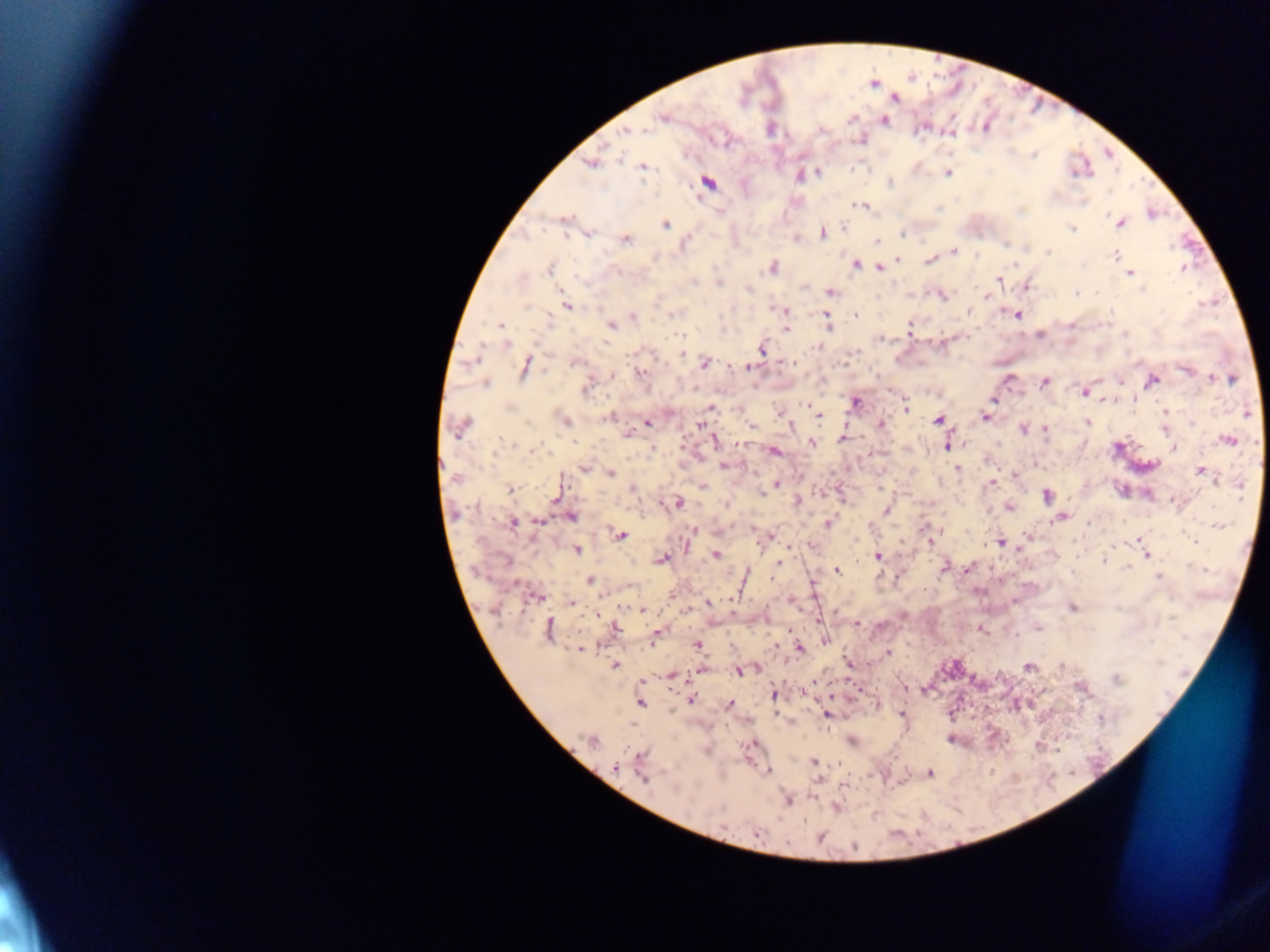

Approximate centers as [x, y] in pixels. Malaria parasite locations: [874, 84], [894, 97], [663, 118], [851, 118], [883, 120], [820, 130], [627, 131], [951, 132], [860, 139], [590, 162], [643, 166], [816, 172], [947, 172], [799, 175], [707, 182], [862, 205], [1151, 213], [564, 221], [1119, 222], [665, 224], [843, 225], [1072, 228], [586, 232], [821, 232], [901, 233], [624, 239], [796, 239], [876, 242], [953, 251], [1115, 255], [930, 259], [898, 260], [854, 264], [772, 267], [878, 267], [550, 268], [1184, 268], [1129, 273], [998, 279], [718, 282], [1027, 286], [830, 292], [941, 294], [987, 297], [566, 305], [783, 311], [968, 312], [856, 314], [1016, 314], [633, 316], [826, 318], [611, 325], [909, 326], [501, 327], [786, 328], [1040, 334], [879, 338], [505, 344], [762, 348], [474, 359], [791, 361], [574, 362], [704, 363], [750, 365], [524, 366], [1187, 369], [641, 373], [612, 375], [1211, 378], [1232, 378], [1009, 379], [1120, 381], [1152, 381], [1044, 382], [485, 384], [587, 385], [1084, 391], [1133, 398], [994, 399], [1103, 401], [855, 402], [709, 407], [906, 407], [781, 412], [1164, 413], [1247, 413], [817, 415], [611, 417], [985, 417], [564, 420], [937, 420], [647, 421], [1087, 423], [1192, 423], [640, 424], [880, 424], [700, 425], [460, 427], [750, 427], [1023, 427], [1045, 429], [628, 433], [842, 438], [1228, 440], [812, 441], [715, 442], [947, 444], [1173, 447], [654, 448], [774, 450], [725, 465], [584, 468], [957, 468], [1201, 471], [608, 473], [1014, 474], [992, 481], [776, 484], [701, 486], [771, 486], [633, 488], [510, 489], [1047, 494], [797, 501], [1176, 502], [675, 503], [726, 504], [1008, 507], [886, 509], [571, 515], [1058, 517], [512, 522], [828, 523], [694, 529], [620, 535], [768, 536], [1138, 538], [930, 540], [1194, 541], [1000, 542], [790, 545], [575, 549], [715, 554], [1146, 554], [878, 555], [661, 558], [1105, 561], [778, 562], [1128, 566], [945, 567], [968, 568], [837, 570], [1158, 575], [590, 580], [812, 588], [537, 595], [790, 599], [708, 602], [571, 603], [1072, 607], [642, 609], [686, 610], [856, 624], [1037, 628], [614, 629], [979, 629], [549, 630], [788, 631], [657, 635], [825, 640], [698, 645], [581, 648], [799, 648], [887, 653], [614, 664], [849, 665], [1061, 665], [1028, 666], [757, 668], [701, 670], [740, 670], [671, 675], [1115, 679], [813, 680], [641, 682], [904, 687], [1080, 687], [803, 692], [773, 694], [830, 697], [690, 698], [640, 702], [876, 704], [729, 705], [827, 714], [901, 715], [789, 720], [950, 738], [591, 740], [850, 740], [752, 744], [1037, 746], [814, 762], [838, 763], [616, 767], [641, 768], [767, 771], [929, 772], [818, 779], [844, 785], [787, 799], [836, 807]. Thick blood smear. Collected in Ghana. Photographed through a microscope with a mobile-phone camera. One field of view. Image is 1270×952 pixels.